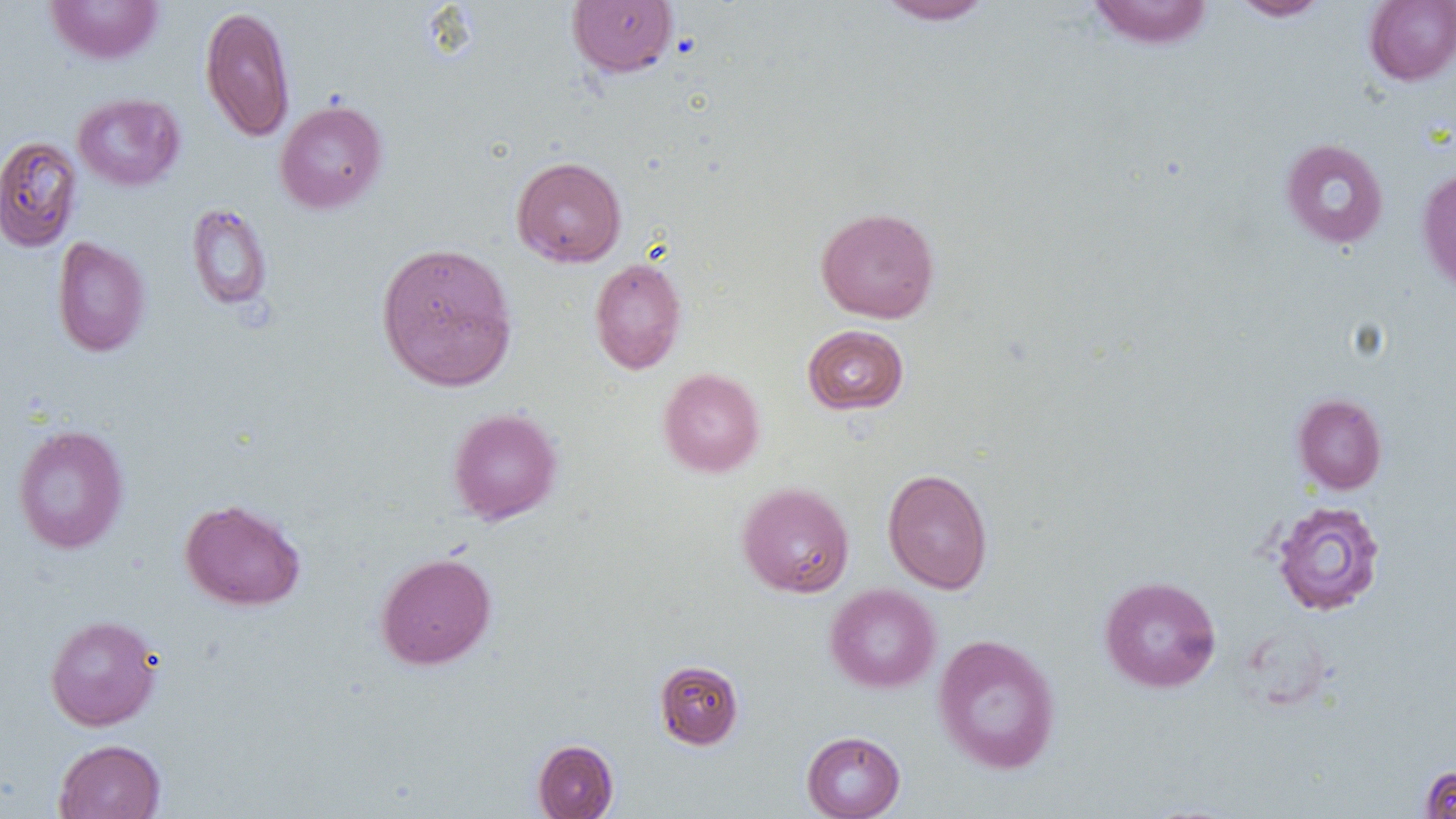

Summary:
  - Coordinate format: approximate bounding boxes as named x1/y1/x2/y2 corners in pixels
  - Uninfected red blood cell locations: (x1=44, y1=0, x2=165, y2=65), (x1=567, y1=0, x2=678, y2=78), (x1=875, y1=0, x2=995, y2=25), (x1=1086, y1=0, x2=1215, y2=50), (x1=1228, y1=0, x2=1332, y2=21), (x1=1363, y1=0, x2=1456, y2=86), (x1=199, y1=5, x2=296, y2=142), (x1=72, y1=93, x2=185, y2=191), (x1=275, y1=100, x2=388, y2=214), (x1=0, y1=135, x2=83, y2=253), (x1=1280, y1=138, x2=1389, y2=249), (x1=511, y1=156, x2=626, y2=267), (x1=1416, y1=164, x2=1456, y2=296), (x1=186, y1=203, x2=273, y2=311), (x1=815, y1=206, x2=940, y2=323), (x1=52, y1=236, x2=151, y2=357), (x1=375, y1=241, x2=518, y2=391), (x1=589, y1=257, x2=687, y2=374), (x1=802, y1=324, x2=909, y2=414), (x1=658, y1=367, x2=765, y2=477), (x1=1292, y1=393, x2=1387, y2=494), (x1=447, y1=407, x2=563, y2=525), (x1=12, y1=424, x2=129, y2=554), (x1=882, y1=468, x2=994, y2=594), (x1=737, y1=482, x2=854, y2=597), (x1=179, y1=498, x2=306, y2=611), (x1=1271, y1=500, x2=1386, y2=616), (x1=375, y1=551, x2=496, y2=670), (x1=1099, y1=575, x2=1221, y2=693), (x1=825, y1=583, x2=941, y2=693), (x1=45, y1=614, x2=162, y2=731), (x1=933, y1=634, x2=1061, y2=774), (x1=654, y1=660, x2=744, y2=749), (x1=801, y1=730, x2=905, y2=819), (x1=53, y1=739, x2=166, y2=818), (x1=533, y1=739, x2=618, y2=818), (x1=1420, y1=765, x2=1456, y2=818)
  - Slide-level diagnosis: negative for blood parasites
  - Field of view: one of a larger specimen
  - Magnification: 1000x
  - Modality: optical microscopy
  - Preparation: thin blood smear
  - Image size: 1456×819 pixels